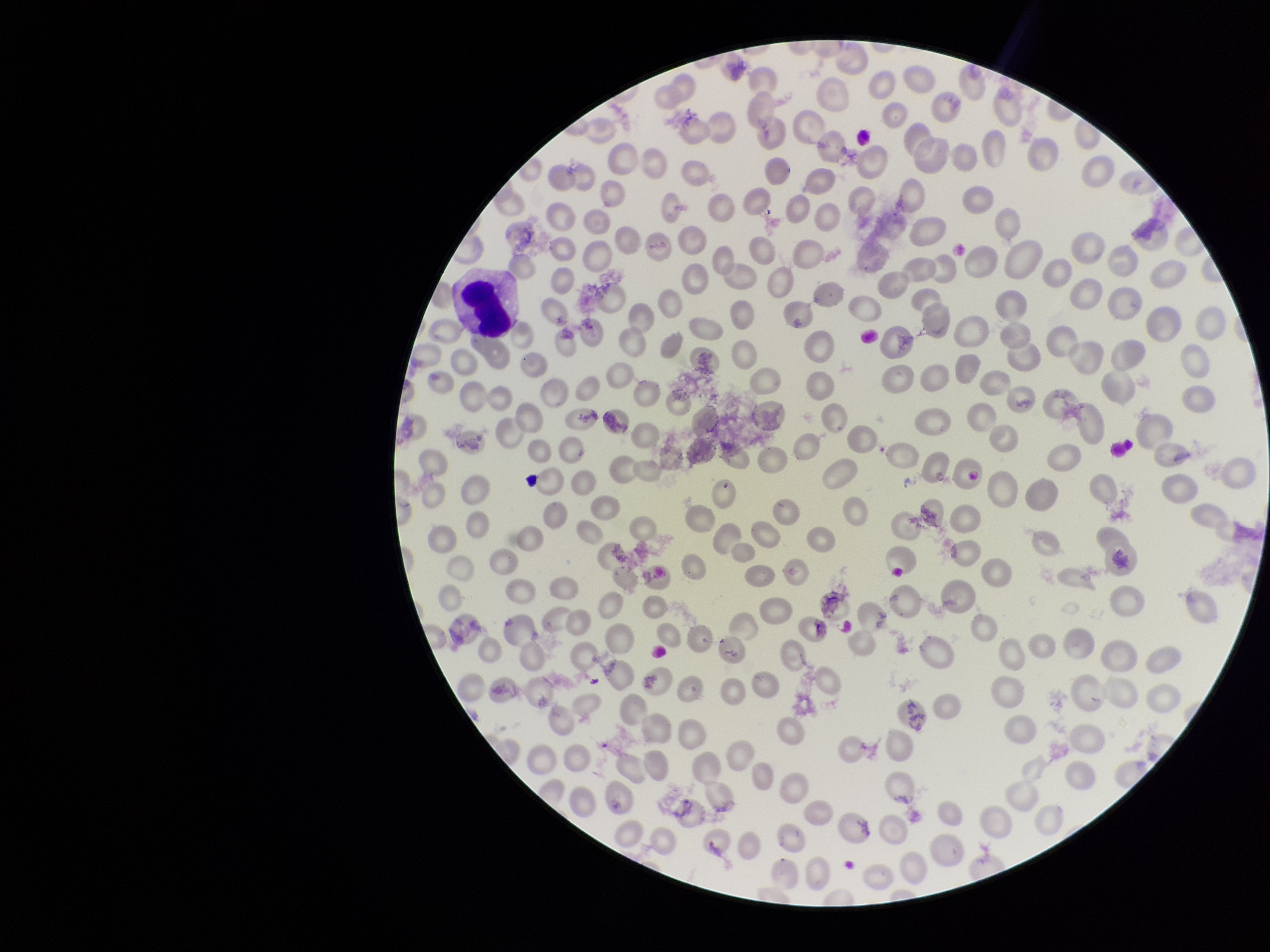
Summary:
  - Parasitized red blood cell count: 0
  - Preparation: thin smear
  - Species reported for this patient: Plasmodium vivax
  - Stain: Giemsa
  - Patient malaria status: infected
  - Image size: 1270×952 pixels
  - Field of view: single
  - Red blood cell count: 254
  - Parasitized red blood cells: none seen
  - Capture: smartphone photograph through the microscope eyepiece